Point out each malaria parasite.
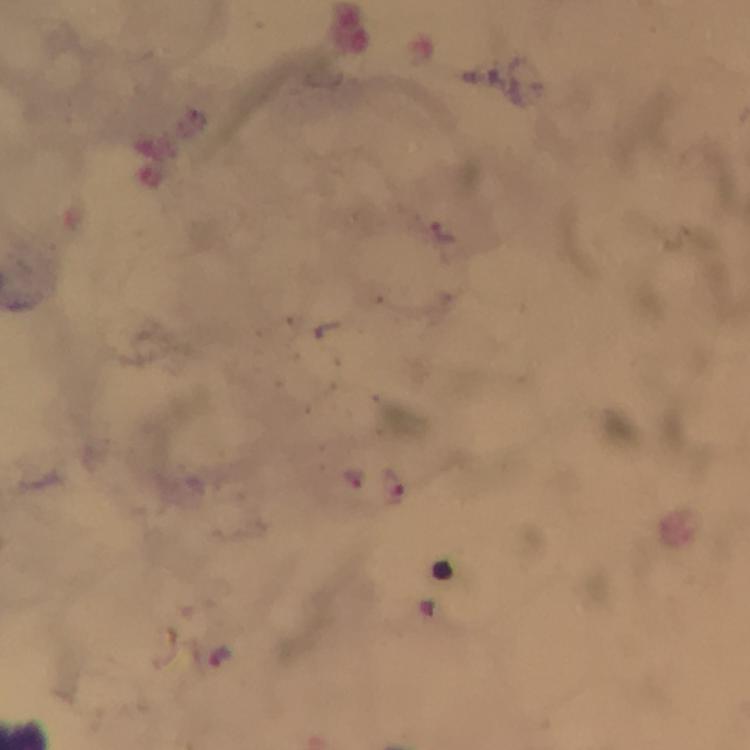

Approximate object centers, in pixels from the top-left corner.
Malaria parasites: (x=442, y=233), (x=355, y=477), (x=396, y=482), (x=221, y=656).

Summary:
  - Preparation: thick blood film
  - Magnification: 100x
  - Cropped from: a single field of view
  - Image size: 750×750 pixels
  - Capture: smartphone mounted on the microscope
  - Stain: Giemsa
  - Context: from a diagnostic examination for malaria
  - Immersion oil: used